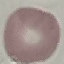
Result: no malaria parasites seen. Cell patch, automatically extracted from a larger field of view and resized to 64 × 64 pixels. Acquired by smartphone through the microscope eyepiece. Thin blood smear. Giemsa stain.